Point out each Plasmodium parasite.
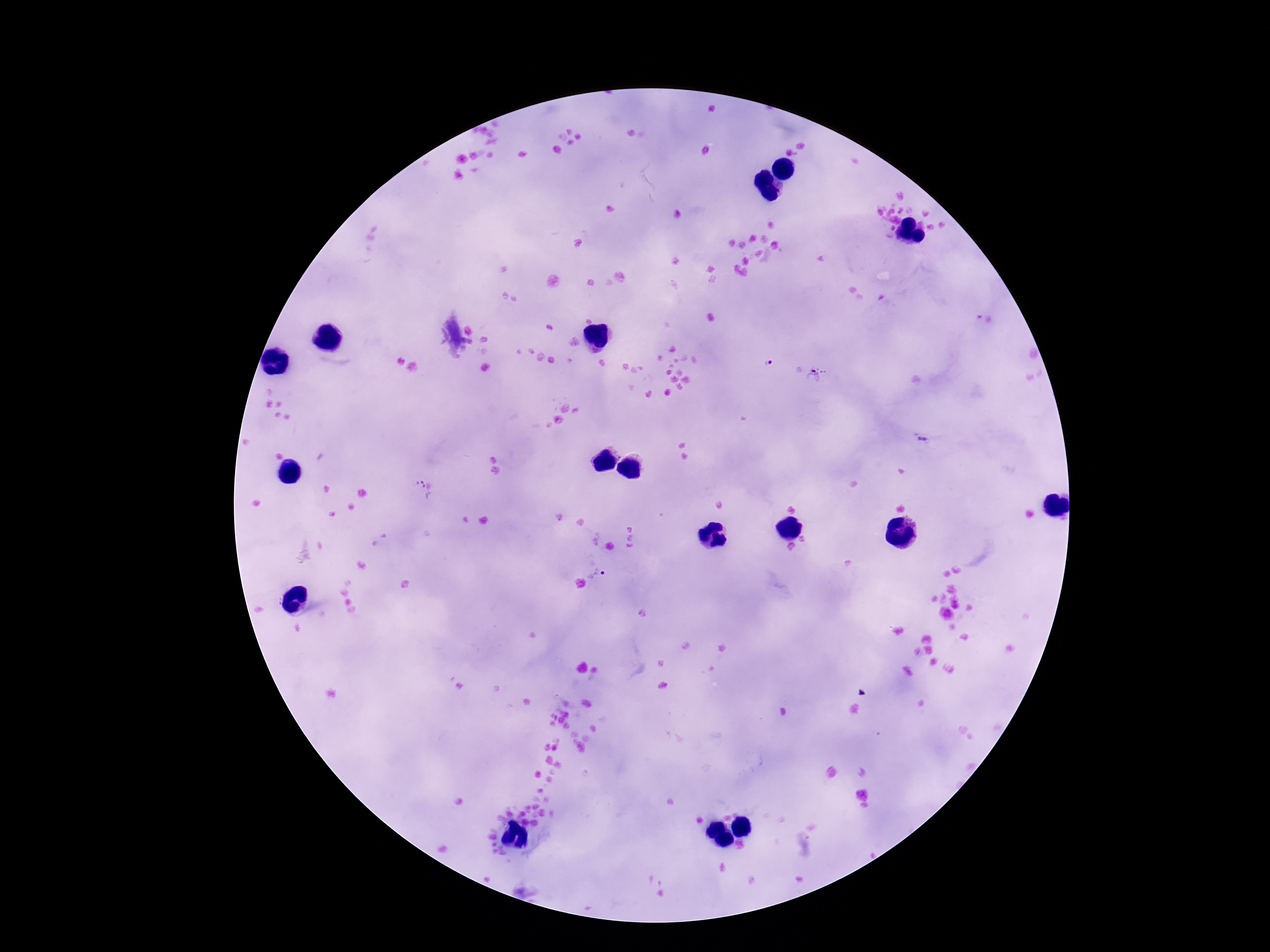
Approximate centers as [x, y] in pixels.
Plasmodium parasites: [769, 362], [814, 376], [922, 438], [420, 490], [597, 574].

Summary:
  - Preparation: thick peripheral-blood smear
  - Patient malaria status: positive
  - Capture: smartphone camera through the microscope eyepiece
  - Field of view: single
  - Magnification: 100x
  - Image size: 1270×952 pixels
  - Stain: Giemsa